Outline each Plasmodium falciparum-infected red blood cell.
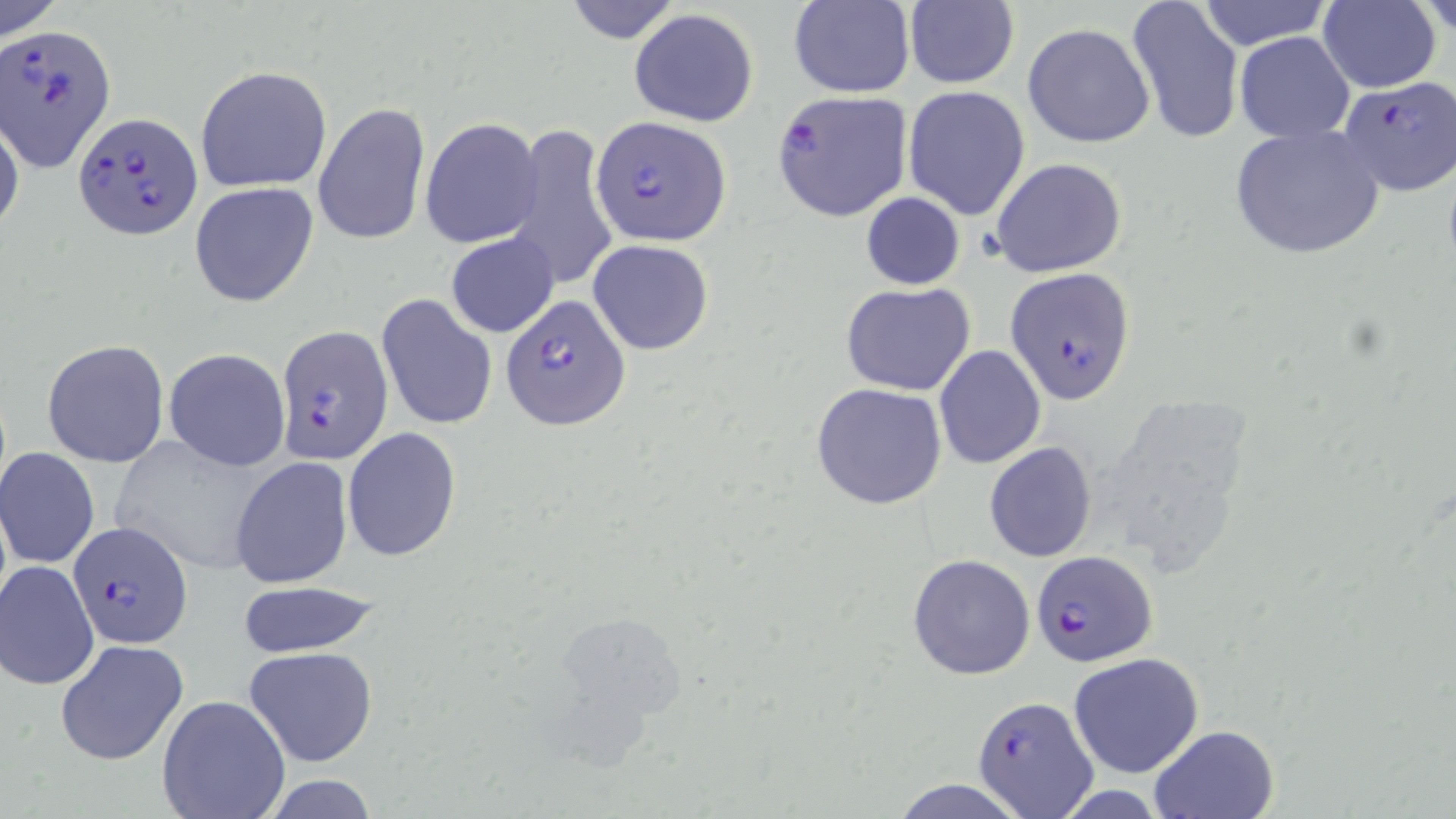

Approximate bounding boxes as named x1/y1/x2/y2 corners in pixels.
Plasmodium falciparum-infected red blood cells: (x1=3, y1=24, x2=116, y2=172), (x1=1337, y1=75, x2=1455, y2=198), (x1=769, y1=89, x2=914, y2=223), (x1=74, y1=110, x2=204, y2=236), (x1=592, y1=114, x2=731, y2=249), (x1=1004, y1=267, x2=1137, y2=405), (x1=504, y1=293, x2=632, y2=430), (x1=276, y1=325, x2=394, y2=467), (x1=70, y1=520, x2=192, y2=647), (x1=1031, y1=550, x2=1157, y2=667), (x1=973, y1=696, x2=1099, y2=815).

slide-level diagnosis = Plasmodium falciparum
modality = light microscopy
magnification = 1000x
stain = May-Grünwald-Giemsa
image size = 1456×819 pixels
uninfected red blood cell locations = approximate bounding boxes as named x1/y1/x2/y2 corners in pixels: (x1=0, y1=0, x2=63, y2=41), (x1=561, y1=0, x2=683, y2=45), (x1=1126, y1=0, x2=1246, y2=146), (x1=1194, y1=0, x2=1333, y2=51), (x1=1318, y1=0, x2=1441, y2=93), (x1=789, y1=1, x2=914, y2=98), (x1=1414, y1=1, x2=1455, y2=38), (x1=901, y1=2, x2=1020, y2=88), (x1=629, y1=8, x2=759, y2=127), (x1=1023, y1=23, x2=1157, y2=149), (x1=1235, y1=32, x2=1355, y2=142), (x1=194, y1=64, x2=332, y2=193), (x1=902, y1=85, x2=1031, y2=220), (x1=312, y1=100, x2=430, y2=247), (x1=0, y1=114, x2=24, y2=239), (x1=419, y1=116, x2=543, y2=248), (x1=505, y1=123, x2=618, y2=290), (x1=1228, y1=123, x2=1385, y2=260), (x1=991, y1=157, x2=1128, y2=277), (x1=189, y1=181, x2=319, y2=308), (x1=860, y1=192, x2=965, y2=290), (x1=445, y1=231, x2=559, y2=338), (x1=586, y1=238, x2=715, y2=356), (x1=841, y1=282, x2=976, y2=395), (x1=377, y1=293, x2=497, y2=432), (x1=41, y1=338, x2=170, y2=469), (x1=934, y1=344, x2=1046, y2=467), (x1=163, y1=347, x2=290, y2=470), (x1=810, y1=381, x2=948, y2=511), (x1=342, y1=427, x2=461, y2=562), (x1=111, y1=435, x2=273, y2=576), (x1=983, y1=442, x2=1097, y2=562), (x1=0, y1=447, x2=100, y2=570), (x1=230, y1=455, x2=354, y2=590), (x1=907, y1=554, x2=1035, y2=679), (x1=1, y1=560, x2=99, y2=690), (x1=230, y1=580, x2=387, y2=659), (x1=55, y1=638, x2=189, y2=766), (x1=244, y1=645, x2=379, y2=769), (x1=1068, y1=652, x2=1204, y2=776), (x1=156, y1=694, x2=291, y2=819), (x1=1147, y1=724, x2=1280, y2=818), (x1=890, y1=779, x2=1029, y2=817)
field of view = one of a larger specimen
preparation = thin blood film